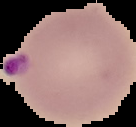

image size = 136×127 pixels
preparation = thin blood smear
malaria status = parasitized
image type = segmented cell region on a black background